Name the parasite shown.
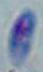
Toxoplasma gondii.

modality: micrograph
magnification: 1000x